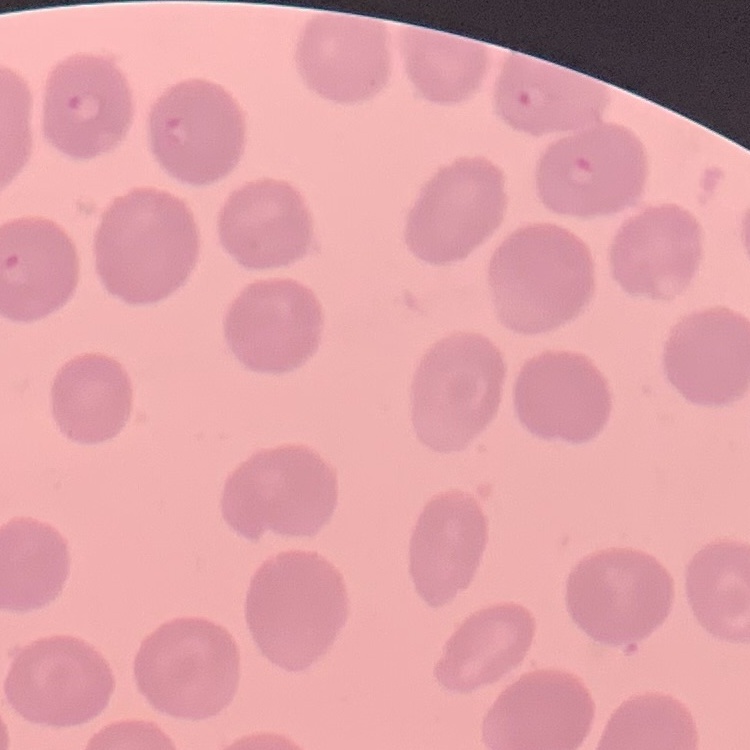
Summary:
  - Red blood cell morphology: no rouleaux formation
  - Image type: one tile cut from a larger photomicrograph
  - Preparation: thin blood smear
  - Stain: Field's or Giemsa